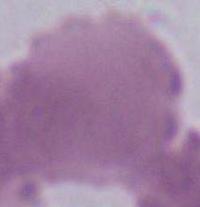

An erythrocyte is seen. Captured at 1000x magnification. Photomicrograph.